Give the extent of all Plasmodium malariae-infected red blood cells.
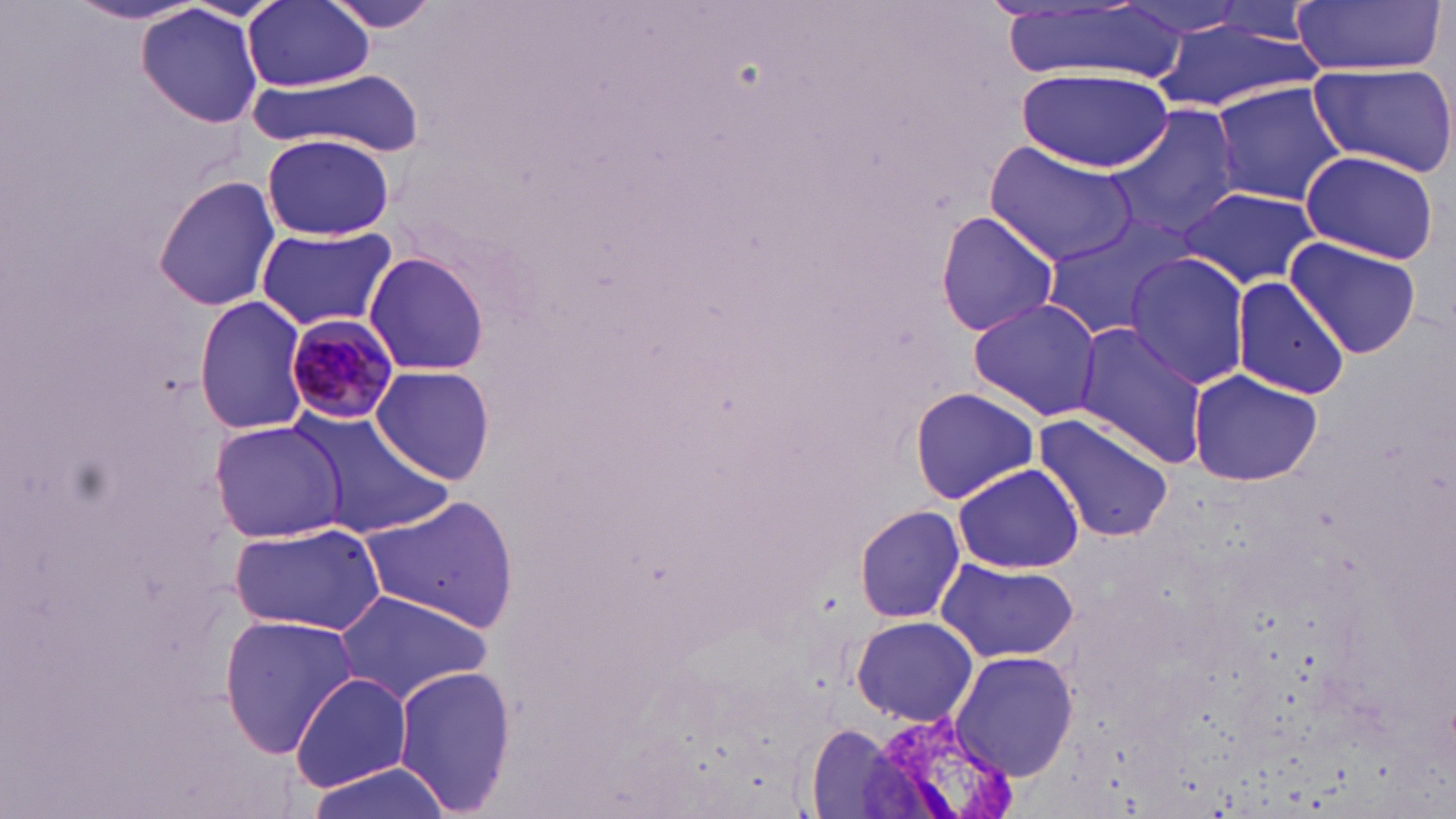

Approximate bounding boxes as [x1, y1, x2, y2] in pixels.
Plasmodium malariae-infected red blood cells: [285, 312, 400, 425].

slide_level_diagnosis: Plasmodium malariae
modality: light microscopy
stain: May-Grünwald-Giemsa
field_of_view: one of a larger specimen
magnification: 1000x
image_size: 1456×819 pixels
uninfected_red_blood_cell_locations: 'approximate bounding boxes as [x1, y1, x2, y2] in pixels: [244, 0, 373, 90], [318, 0, 444, 34], [1290, 0, 1446, 76], [1119, 1, 1252, 40], [66, 2, 211, 25], [1207, 3, 1322, 41], [995, 4, 1178, 81], [137, 6, 265, 128], [1152, 21, 1320, 111], [1306, 60, 1456, 176], [247, 66, 425, 155], [1017, 66, 1174, 174], [1209, 82, 1348, 205], [1106, 105, 1244, 241], [261, 132, 395, 241], [986, 141, 1139, 265], [1299, 148, 1441, 264], [154, 175, 281, 312], [1175, 187, 1320, 290], [933, 210, 1059, 337], [1037, 222, 1185, 340], [255, 224, 399, 333], [1284, 236, 1425, 359], [364, 248, 490, 379], [1125, 252, 1250, 390], [1230, 278, 1352, 399], [193, 295, 309, 434], [966, 298, 1103, 421], [1070, 322, 1211, 468], [371, 364, 496, 486], [1186, 369, 1323, 488], [908, 386, 1040, 503], [286, 408, 454, 538], [1031, 412, 1177, 540], [208, 419, 344, 543], [951, 462, 1087, 570], [359, 493, 520, 633], [856, 505, 968, 623], [228, 520, 386, 636], [936, 558, 1080, 663], [329, 588, 494, 705], [218, 613, 359, 759], [850, 616, 980, 728], [949, 649, 1078, 780], [392, 662, 515, 818], [289, 672, 412, 792], [803, 724, 909, 816], [299, 763, 450, 819]'
preparation: thin blood film